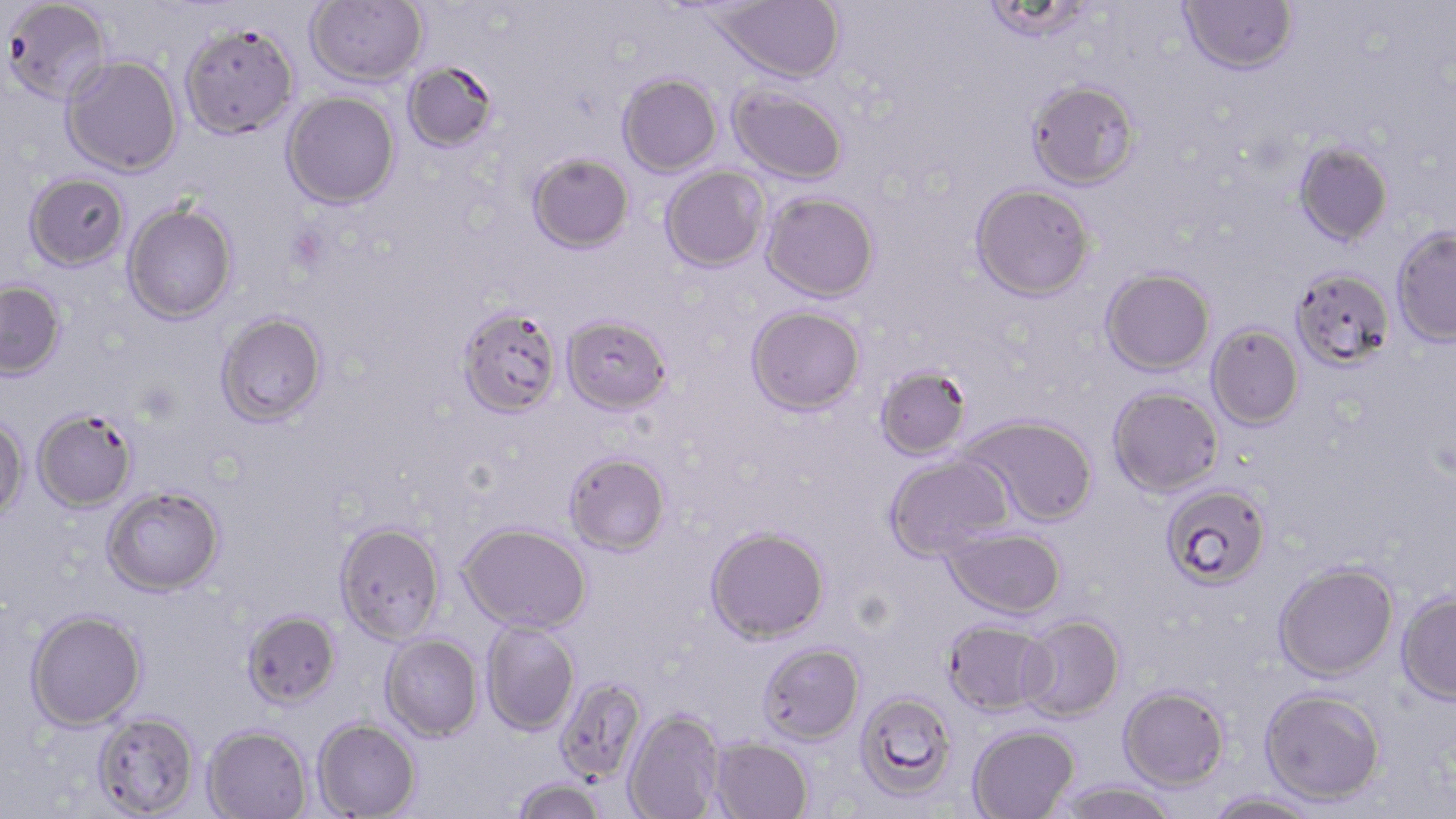

slide-level diagnosis = Plasmodium falciparum
modality = light microscopy
uninfected red blood cell locations = approximate bounding boxes as named x1/y1/x2/y2 corners in pixels: (x1=2, y1=0, x2=112, y2=105), (x1=305, y1=0, x2=427, y2=87), (x1=708, y1=0, x2=845, y2=83), (x1=1179, y1=0, x2=1298, y2=75), (x1=982, y1=1, x2=1095, y2=44), (x1=179, y1=22, x2=299, y2=139), (x1=61, y1=55, x2=183, y2=177), (x1=403, y1=61, x2=500, y2=153), (x1=617, y1=73, x2=722, y2=177), (x1=1026, y1=79, x2=1141, y2=190), (x1=728, y1=84, x2=848, y2=184), (x1=281, y1=91, x2=400, y2=209), (x1=1293, y1=139, x2=1393, y2=246), (x1=527, y1=152, x2=634, y2=253), (x1=660, y1=166, x2=769, y2=272), (x1=24, y1=173, x2=130, y2=271), (x1=970, y1=183, x2=1095, y2=301), (x1=761, y1=192, x2=879, y2=301), (x1=123, y1=201, x2=237, y2=325), (x1=1391, y1=226, x2=1456, y2=346), (x1=1101, y1=267, x2=1215, y2=375), (x1=1290, y1=267, x2=1395, y2=370), (x1=0, y1=281, x2=66, y2=380), (x1=746, y1=305, x2=865, y2=415), (x1=456, y1=306, x2=563, y2=417), (x1=216, y1=311, x2=328, y2=427), (x1=562, y1=314, x2=671, y2=414), (x1=1206, y1=323, x2=1304, y2=430), (x1=874, y1=363, x2=972, y2=460), (x1=1108, y1=385, x2=1224, y2=497), (x1=33, y1=409, x2=137, y2=512), (x1=0, y1=415, x2=28, y2=519), (x1=962, y1=415, x2=1098, y2=526), (x1=563, y1=451, x2=671, y2=555), (x1=884, y1=452, x2=1013, y2=560), (x1=1161, y1=483, x2=1272, y2=589), (x1=101, y1=485, x2=225, y2=596), (x1=334, y1=521, x2=445, y2=644), (x1=459, y1=522, x2=591, y2=633), (x1=705, y1=526, x2=829, y2=643), (x1=943, y1=526, x2=1067, y2=618), (x1=1273, y1=561, x2=1398, y2=682), (x1=1396, y1=589, x2=1456, y2=704), (x1=26, y1=609, x2=147, y2=730), (x1=242, y1=610, x2=341, y2=710), (x1=1017, y1=615, x2=1125, y2=722), (x1=942, y1=618, x2=1055, y2=716), (x1=481, y1=621, x2=580, y2=735), (x1=380, y1=634, x2=484, y2=741), (x1=757, y1=642, x2=864, y2=744), (x1=554, y1=676, x2=647, y2=784), (x1=1118, y1=685, x2=1230, y2=791), (x1=1259, y1=687, x2=1385, y2=806), (x1=854, y1=690, x2=957, y2=801), (x1=623, y1=708, x2=724, y2=819), (x1=92, y1=711, x2=200, y2=818), (x1=312, y1=718, x2=421, y2=818), (x1=201, y1=724, x2=312, y2=819), (x1=967, y1=725, x2=1079, y2=819), (x1=710, y1=737, x2=813, y2=819), (x1=510, y1=777, x2=608, y2=819), (x1=1054, y1=780, x2=1180, y2=819), (x1=1205, y1=791, x2=1326, y2=819)
field of view = one of a larger specimen
image size = 1456×819 pixels
magnification = 1000x
stain = May-Grünwald-Giemsa
preparation = thin blood film